Give the extent of all Trypanosoma brucei.
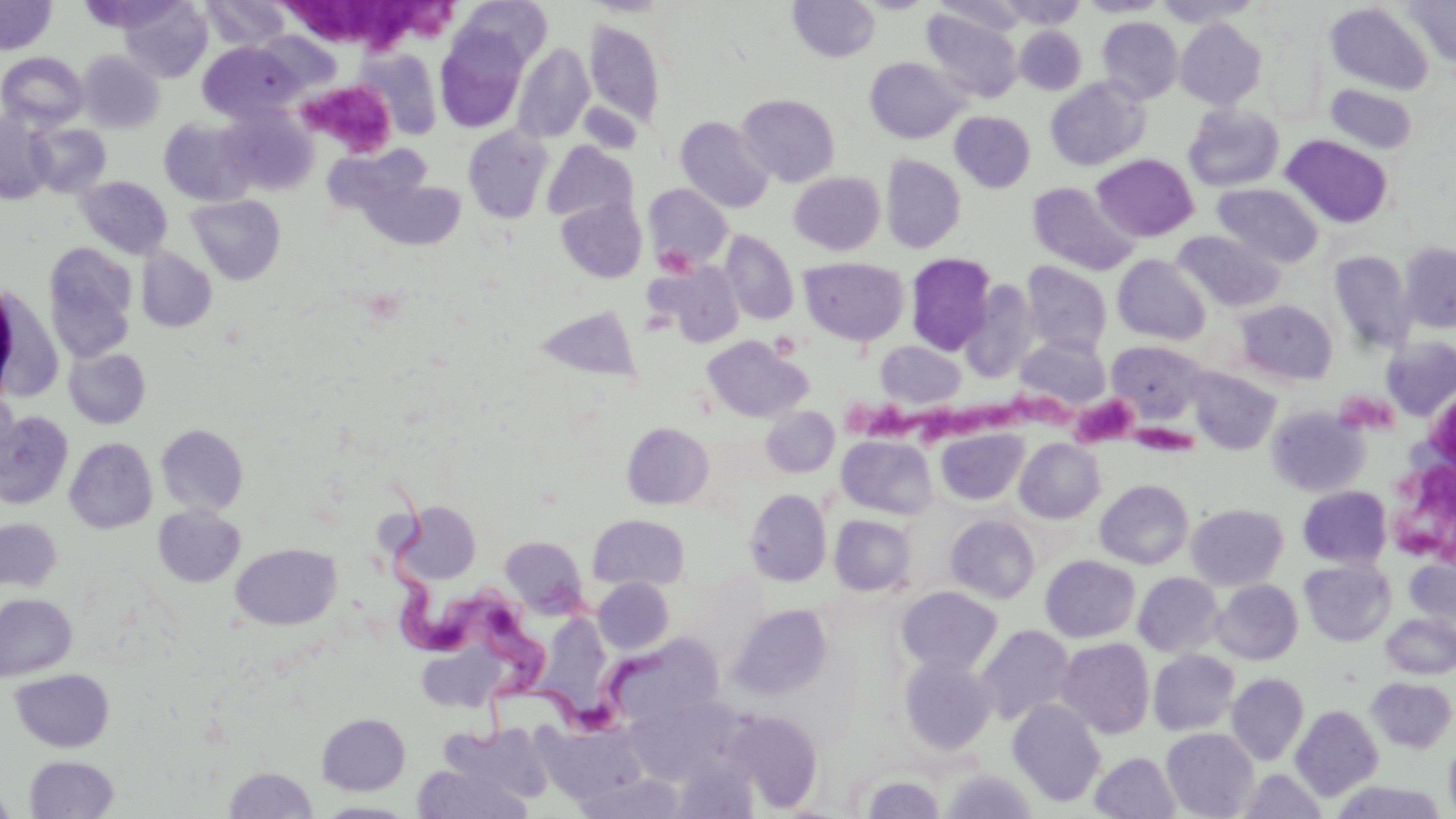

Approximate bounding boxes as (x1,y1)-(x2,y2) corner pairs in pixels.
Trypanosoma brucei: (374,472)-(550,702), (471,645)-(680,761).

Platelet locations: (290,0)-(456,56), (306,82)-(397,155), (655,244)-(694,276), (1335,388)-(1396,435), (1009,391)-(1085,440), (1074,396)-(1144,448), (975,399)-(1020,440), (847,400)-(926,440), (1426,401)-(1455,458), (924,404)-(984,451), (1130,419)-(1197,459), (1389,455)-(1453,562). Uninfected red blood cell locations: (0,0)-(56,54), (456,0)-(551,70), (583,0)-(674,17), (787,0)-(880,62), (999,0)-(1089,29), (1077,0)-(1169,17), (1155,0)-(1261,27), (1404,0)-(1456,70), (77,1)-(182,30), (119,1)-(213,83), (202,1)-(291,51), (1325,3)-(1434,95), (921,9)-(1023,102), (1097,16)-(1183,103), (1175,18)-(1267,109), (585,19)-(665,128), (1015,26)-(1086,95), (435,29)-(529,133), (255,31)-(340,95), (1261,41)-(1327,124), (198,42)-(301,121), (513,43)-(594,143), (359,49)-(442,139), (78,51)-(164,133), (0,52)-(88,128), (865,57)-(965,143), (1045,77)-(1149,171), (1326,83)-(1417,154), (737,94)-(841,187), (1182,105)-(1285,193), (221,106)-(317,195), (950,111)-(1036,193), (0,113)-(56,205), (675,116)-(774,213), (159,118)-(257,205), (28,123)-(112,197), (463,126)-(554,223), (1280,135)-(1393,229), (542,141)-(638,225), (324,142)-(432,214), (1092,154)-(1199,242), (880,155)-(966,253), (789,172)-(885,255), (76,176)-(172,259), (358,177)-(466,250), (1027,182)-(1140,275), (1212,183)-(1324,268), (644,184)-(733,271), (187,195)-(285,285), (556,197)-(647,283), (1173,230)-(1286,313), (721,231)-(799,325), (1399,241)-(1456,333), (43,244)-(138,362), (136,248)-(217,332), (1330,251)-(1414,352), (905,253)-(996,355), (1112,254)-(1211,345), (799,256)-(909,346), (653,261)-(744,348), (1021,261)-(1112,355), (961,280)-(1039,382), (0,286)-(63,402), (1234,299)-(1338,386), (534,305)-(639,382), (1015,334)-(1111,411), (701,335)-(812,422), (1381,337)-(1456,421), (875,340)-(966,409), (1106,340)-(1209,422), (64,348)-(151,429), (1186,367)-(1281,454), (0,388)-(19,480), (1266,405)-(1369,496), (760,406)-(840,477), (0,412)-(74,509), (621,422)-(715,510), (156,424)-(249,516), (936,429)-(1028,505), (838,436)-(937,519), (65,437)-(158,533), (1015,439)-(1105,523), (1095,480)-(1193,569), (1297,485)-(1391,568), (745,488)-(832,586), (395,502)-(481,584), (1186,504)-(1288,589), (152,505)-(245,587), (588,514)-(689,590), (829,514)-(915,596), (945,514)-(1040,604), (0,518)-(62,592), (500,535)-(589,616), (230,544)-(341,630), (1040,555)-(1140,642), (1405,556)-(1456,636), (1299,559)-(1395,646), (1133,572)-(1224,658), (593,577)-(674,654), (1211,580)-(1303,665), (896,586)-(1002,675), (0,593)-(77,681), (729,604)-(832,700), (1381,614)-(1456,678), (976,625)-(1075,725), (610,634)-(723,727), (1057,637)-(1155,739), (415,640)-(508,711), (1148,649)-(1240,736), (897,654)-(997,755), (10,669)-(114,752), (1227,673)-(1309,765), (1367,677)-(1455,753), (627,694)-(736,784), (1007,700)-(1106,806), (1291,705)-(1384,801), (728,710)-(822,811), (316,713)-(410,795), (537,723)-(645,805), (435,724)-(556,806), (1162,728)-(1258,818), (1443,733)-(1456,819), (1089,751)-(1182,818), (24,755)-(119,818), (675,756)-(758,819), (412,764)-(532,819), (223,766)-(318,818), (939,769)-(1038,818), (1238,769)-(1327,818), (574,772)-(684,818), (859,774)-(944,818), (1330,781)-(1448,818), (0,787)-(17,818), (315,801)-(419,818). Slide-level diagnosis: Trypanosoma brucei. May-Grünwald-Giemsa stain. Thin blood smear. 1000x magnification. Image is 1456×819 pixels. One field of a larger specimen. Light microscopy.